Locate every blood parasite and identify its species.
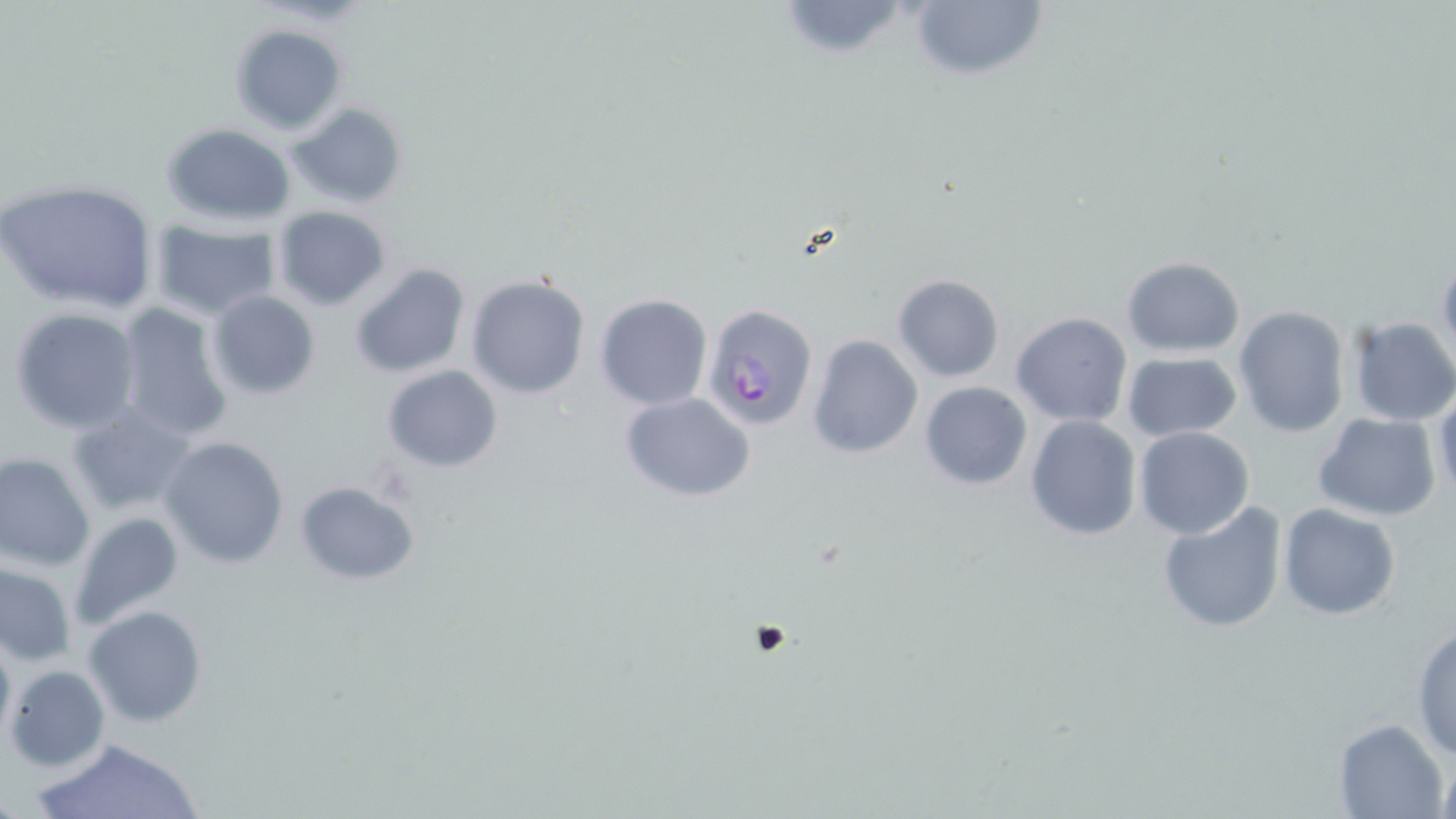

Approximate bounding boxes as named x1/y1/x2/y2 corners in pixels.
Plasmodium falciparum-infected red blood cells: (x1=702, y1=303, x2=819, y2=432).
No Plasmodium ovale, Plasmodium malariae, Plasmodium vivax, Babesia divergens, or Trypanosoma brucei observed.

Uninfected red blood cell locations: (x1=905, y1=0, x2=1049, y2=85), (x1=775, y1=1, x2=911, y2=61), (x1=229, y1=23, x2=349, y2=135), (x1=285, y1=102, x2=409, y2=208), (x1=161, y1=124, x2=297, y2=227), (x1=0, y1=178, x2=162, y2=313), (x1=272, y1=204, x2=392, y2=311), (x1=148, y1=221, x2=281, y2=319), (x1=1120, y1=255, x2=1244, y2=355), (x1=1436, y1=256, x2=1456, y2=367), (x1=349, y1=263, x2=472, y2=381), (x1=892, y1=274, x2=1004, y2=383), (x1=465, y1=275, x2=590, y2=399), (x1=206, y1=289, x2=320, y2=400), (x1=593, y1=294, x2=711, y2=410), (x1=114, y1=303, x2=233, y2=444), (x1=8, y1=306, x2=142, y2=434), (x1=1232, y1=307, x2=1351, y2=437), (x1=1010, y1=313, x2=1133, y2=427), (x1=1346, y1=317, x2=1456, y2=427), (x1=805, y1=334, x2=923, y2=461), (x1=1120, y1=353, x2=1242, y2=442), (x1=380, y1=365, x2=503, y2=473), (x1=917, y1=381, x2=1033, y2=490), (x1=1431, y1=388, x2=1456, y2=508), (x1=619, y1=392, x2=757, y2=502), (x1=66, y1=403, x2=197, y2=517), (x1=1313, y1=413, x2=1441, y2=523), (x1=1025, y1=415, x2=1142, y2=540), (x1=1134, y1=427, x2=1255, y2=541), (x1=159, y1=437, x2=290, y2=570), (x1=0, y1=452, x2=97, y2=571), (x1=294, y1=480, x2=420, y2=585), (x1=1156, y1=501, x2=1290, y2=635), (x1=1277, y1=503, x2=1401, y2=620), (x1=70, y1=512, x2=185, y2=631), (x1=0, y1=563, x2=76, y2=666), (x1=83, y1=604, x2=210, y2=726), (x1=1411, y1=622, x2=1456, y2=761), (x1=0, y1=629, x2=14, y2=747), (x1=6, y1=664, x2=111, y2=772), (x1=1332, y1=718, x2=1450, y2=818), (x1=31, y1=736, x2=205, y2=819), (x1=1432, y1=752, x2=1454, y2=816). Platelet locations: (x1=751, y1=622, x2=791, y2=658). Slide-level diagnosis: Plasmodium falciparum. May-Grünwald-Giemsa-stained preparation. Thin blood film. One field of a larger specimen. Image is 1456×819 pixels. 1000x magnification. Optical microscopy.